Locate every Plasmodium falciparum-infected red blood cell.
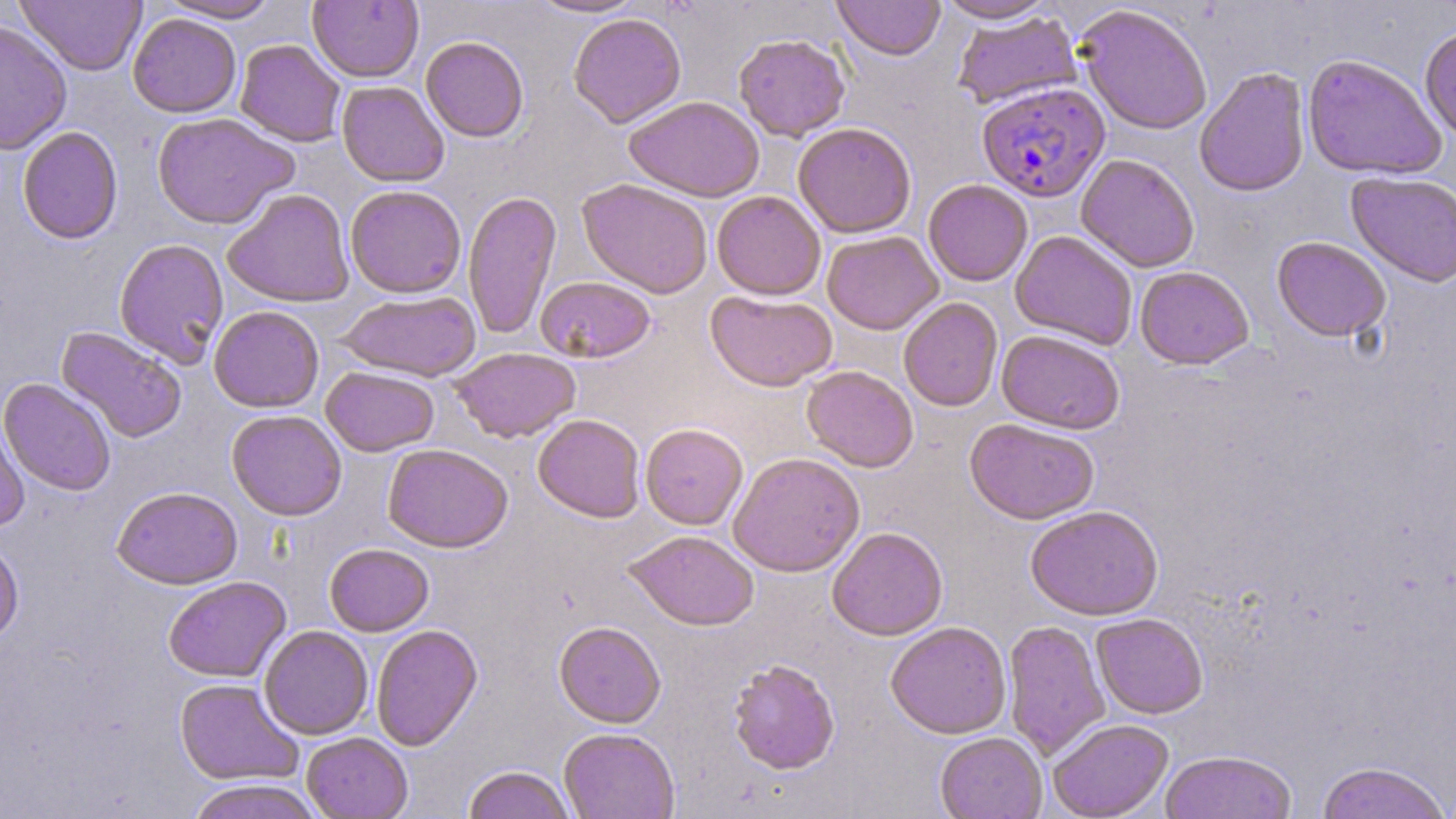

Approximate bounding boxes as (x1,y1)-(x2,y2) corner pairs in pixels.
Plasmodium falciparum-infected red blood cells: (976,81)-(1110,202).

Summary:
  - Uninfected red blood cell locations: (528,0)-(645,18), (832,0)-(945,61), (934,0)-(1057,23), (14,1)-(147,75), (158,1)-(281,22), (308,1)-(424,83), (1076,4)-(1213,135), (952,11)-(1082,109), (128,13)-(241,118), (568,13)-(686,128), (0,18)-(72,155), (1419,25)-(1456,144), (734,33)-(850,141), (421,35)-(529,142), (235,40)-(346,147), (1302,53)-(1448,181), (1194,66)-(1311,197), (337,81)-(449,187), (625,95)-(764,202), (151,111)-(298,230), (793,122)-(916,239), (17,126)-(123,243), (1076,154)-(1200,272), (1345,172)-(1456,288), (576,178)-(713,298), (923,179)-(1033,286), (345,184)-(466,298), (222,188)-(355,308), (463,190)-(562,341), (711,191)-(826,300), (822,230)-(943,335), (1010,230)-(1138,351), (1271,236)-(1391,343), (114,238)-(229,368), (1135,266)-(1254,370), (536,275)-(656,363), (705,290)-(838,392), (338,291)-(482,381), (898,298)-(1003,412), (208,305)-(324,413), (56,327)-(188,443), (996,330)-(1125,434), (450,347)-(581,443), (802,365)-(919,472), (321,366)-(439,457), (1,378)-(116,496), (226,410)-(347,521), (0,413)-(30,531), (533,414)-(645,522), (964,418)-(1100,524), (640,422)-(748,530), (382,443)-(513,552), (728,452)-(865,577), (112,485)-(243,589), (1025,504)-(1163,621), (826,527)-(948,641), (623,530)-(759,631), (0,539)-(23,645), (324,543)-(434,636), (163,576)-(291,682), (1091,613)-(1209,719), (1002,620)-(1110,759), (554,621)-(666,727), (886,621)-(1012,740), (370,623)-(483,751), (259,625)-(373,740), (728,659)-(840,775), (174,678)-(303,786), (1048,719)-(1173,819), (559,727)-(679,817), (301,732)-(412,818), (935,732)-(1047,819), (1159,750)-(1297,819), (1315,761)-(1451,819), (462,765)-(577,819), (184,779)-(327,819)
  - Slide-level diagnosis: Plasmodium falciparum
  - Stain: May-Grünwald-Giemsa
  - Image size: 1456×819 pixels
  - Magnification: 1000x
  - Modality: optical microscopy
  - Field of view: single
  - Preparation: thin blood smear